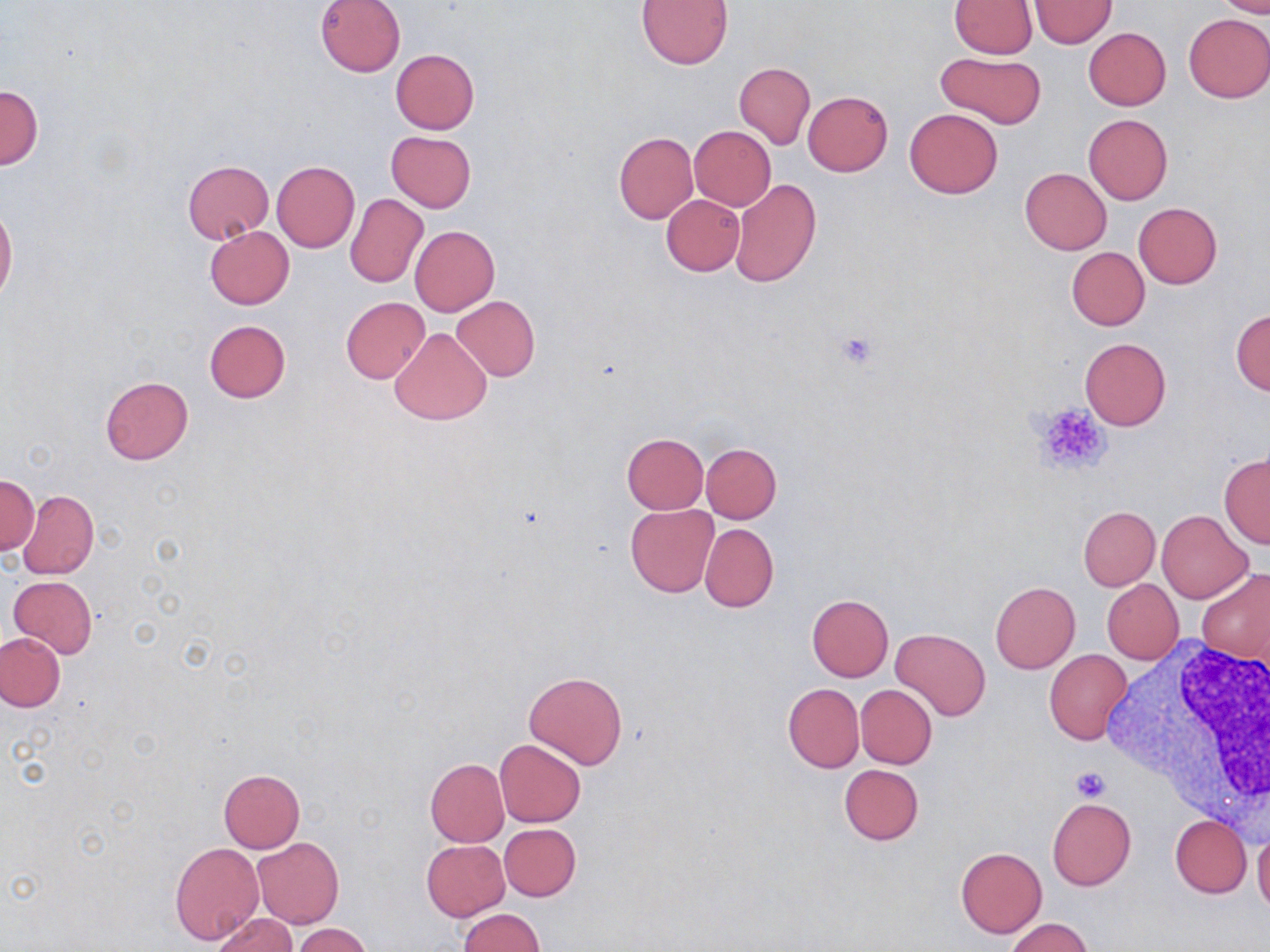
Approximate bounding boxes as named x1/y1/x2/y2 corners in pixels. White blood cell locations: (x1=1105, y1=635, x2=1270, y2=826). Uninfected red blood cell locations: (x1=315, y1=0, x2=406, y2=77), (x1=638, y1=0, x2=733, y2=68), (x1=949, y1=0, x2=1037, y2=57), (x1=1214, y1=0, x2=1270, y2=17), (x1=1030, y1=1, x2=1115, y2=48), (x1=1183, y1=13, x2=1270, y2=103), (x1=1083, y1=27, x2=1170, y2=110), (x1=390, y1=49, x2=479, y2=134), (x1=934, y1=51, x2=1046, y2=129), (x1=733, y1=63, x2=815, y2=150), (x1=0, y1=84, x2=43, y2=170), (x1=803, y1=90, x2=893, y2=176), (x1=904, y1=108, x2=1002, y2=199), (x1=1083, y1=114, x2=1173, y2=204), (x1=689, y1=126, x2=776, y2=211), (x1=386, y1=131, x2=476, y2=212), (x1=613, y1=131, x2=697, y2=224), (x1=182, y1=160, x2=274, y2=243), (x1=272, y1=161, x2=359, y2=252), (x1=1020, y1=168, x2=1112, y2=255), (x1=729, y1=178, x2=821, y2=287), (x1=662, y1=194, x2=744, y2=275), (x1=345, y1=195, x2=428, y2=287), (x1=1133, y1=202, x2=1223, y2=289), (x1=0, y1=203, x2=17, y2=306), (x1=205, y1=225, x2=294, y2=309), (x1=409, y1=225, x2=499, y2=315), (x1=1066, y1=247, x2=1149, y2=331), (x1=451, y1=295, x2=540, y2=382), (x1=341, y1=297, x2=429, y2=384), (x1=1231, y1=308, x2=1270, y2=397), (x1=204, y1=319, x2=291, y2=402), (x1=388, y1=328, x2=491, y2=425), (x1=1080, y1=337, x2=1171, y2=431), (x1=99, y1=376, x2=193, y2=465), (x1=620, y1=433, x2=708, y2=513), (x1=701, y1=443, x2=781, y2=523), (x1=1220, y1=452, x2=1270, y2=550), (x1=1, y1=476, x2=38, y2=554), (x1=18, y1=491, x2=99, y2=579), (x1=626, y1=504, x2=718, y2=597), (x1=1078, y1=505, x2=1160, y2=590), (x1=1157, y1=511, x2=1252, y2=603), (x1=700, y1=523, x2=779, y2=612), (x1=1198, y1=568, x2=1270, y2=666), (x1=8, y1=575, x2=97, y2=659), (x1=1101, y1=579, x2=1184, y2=665), (x1=989, y1=582, x2=1080, y2=674), (x1=806, y1=594, x2=894, y2=682), (x1=890, y1=628, x2=991, y2=721), (x1=0, y1=632, x2=66, y2=712), (x1=1044, y1=649, x2=1132, y2=745), (x1=524, y1=671, x2=627, y2=770), (x1=782, y1=683, x2=863, y2=772), (x1=855, y1=684, x2=937, y2=768), (x1=495, y1=740, x2=586, y2=827), (x1=424, y1=758, x2=509, y2=847), (x1=838, y1=764, x2=924, y2=845), (x1=218, y1=768, x2=305, y2=852), (x1=1046, y1=796, x2=1136, y2=891), (x1=1171, y1=815, x2=1252, y2=897), (x1=499, y1=823, x2=581, y2=901), (x1=1253, y1=827, x2=1270, y2=918), (x1=252, y1=837, x2=344, y2=929), (x1=421, y1=840, x2=510, y2=921), (x1=170, y1=842, x2=264, y2=945), (x1=956, y1=847, x2=1047, y2=938), (x1=458, y1=908, x2=545, y2=951), (x1=211, y1=912, x2=296, y2=952), (x1=1004, y1=918, x2=1094, y2=952), (x1=293, y1=924, x2=372, y2=952). Platelet locations: (x1=833, y1=329, x2=883, y2=372), (x1=1030, y1=401, x2=1112, y2=475), (x1=1069, y1=766, x2=1113, y2=802). Slide-level diagnosis: no evidence of blood parasites. Single field of view. Image is 1270×952 pixels. Captured at 1000x magnification. Light microscopy. Thin blood smear. May-Grünwald-Giemsa stain.